Name the blood parasite species.
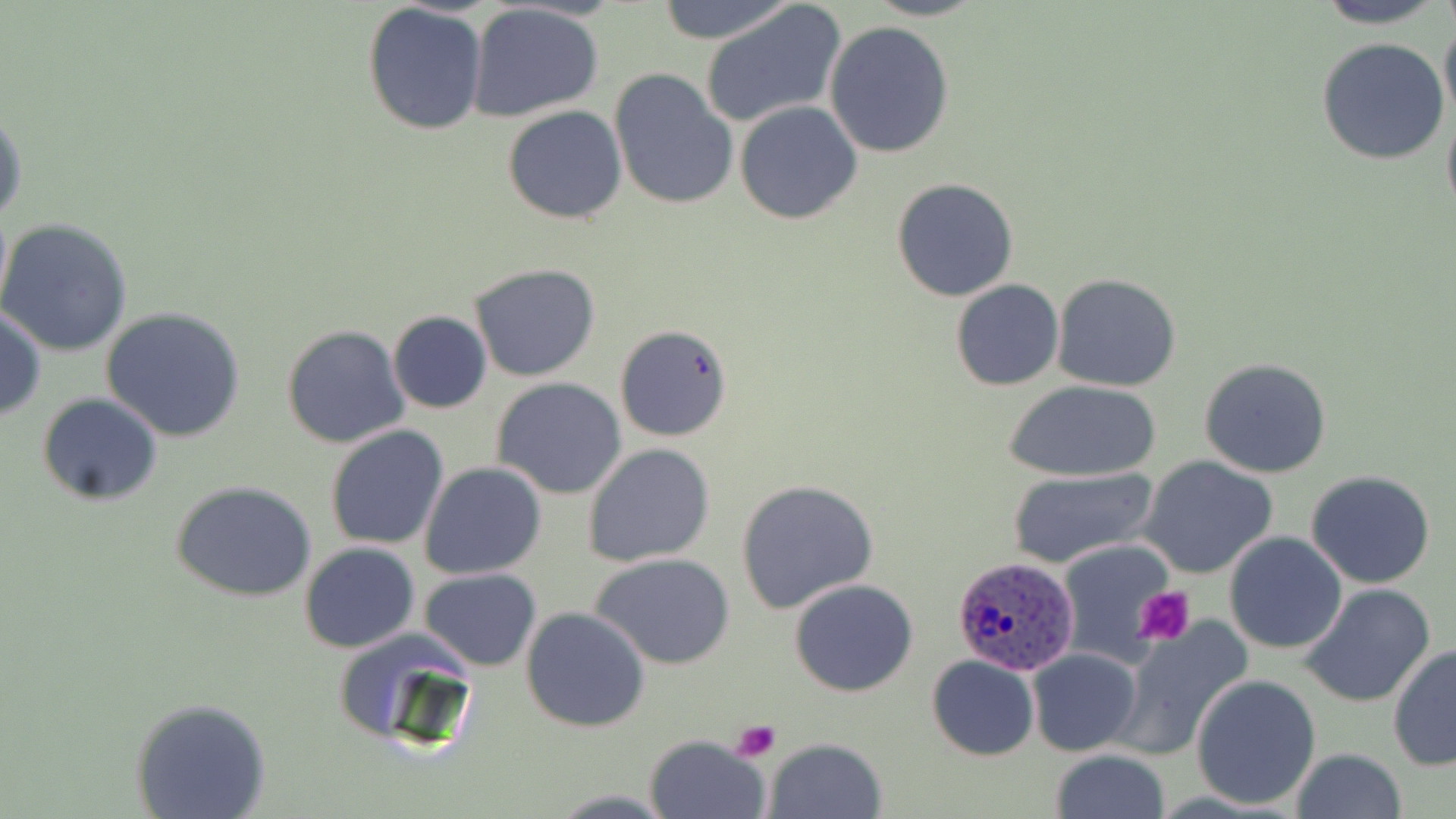
Plasmodium ovale.

image size = 1456×819 pixels
uninfected red blood cell locations = approximate bounding boxes as (x1, y1, x2, y2) in pixels: (653, 0, 795, 45), (863, 0, 988, 21), (1308, 0, 1451, 29), (700, 1, 847, 130), (361, 3, 489, 135), (465, 4, 604, 121), (1439, 16, 1456, 125), (824, 20, 955, 159), (1316, 37, 1450, 165), (609, 69, 739, 210), (734, 101, 863, 225), (1441, 104, 1456, 224), (503, 105, 628, 224), (0, 109, 26, 226), (891, 178, 1020, 301), (0, 218, 134, 357), (468, 263, 602, 383), (1051, 273, 1180, 391), (950, 279, 1064, 391), (0, 306, 45, 420), (99, 308, 247, 444), (388, 311, 492, 414), (282, 323, 410, 448), (614, 324, 734, 442), (1199, 357, 1332, 478), (492, 379, 627, 499), (1005, 380, 1161, 483), (37, 392, 163, 507), (324, 425, 450, 550), (583, 444, 716, 567), (1138, 455, 1279, 580), (419, 462, 548, 581), (1006, 468, 1159, 570), (1305, 471, 1437, 589), (735, 479, 880, 616), (171, 480, 318, 603), (1223, 531, 1348, 656), (1058, 541, 1178, 661), (298, 542, 420, 654), (590, 553, 738, 672), (420, 568, 542, 670), (789, 579, 919, 697), (1301, 583, 1437, 708), (519, 606, 652, 733), (1112, 621, 1251, 760), (332, 626, 484, 754), (1388, 644, 1456, 774), (1026, 647, 1143, 757), (926, 655, 1039, 760), (1190, 674, 1321, 810), (131, 697, 272, 818), (643, 734, 770, 819), (764, 736, 888, 818), (1049, 749, 1171, 819), (1289, 749, 1408, 819)
modality = optical microscopy
Plasmodium ovale-infected red blood cell locations = approximate bounding boxes as (x1, y1, x2, y2) in pixels: (951, 554, 1080, 675)
magnification = 1000x
stain = May-Grünwald-Giemsa
preparation = thin blood film
platelet locations = approximate bounding boxes as (x1, y1, x2, y2) in pixels: (1134, 586, 1196, 648), (730, 718, 782, 763)
field of view = one of a larger specimen